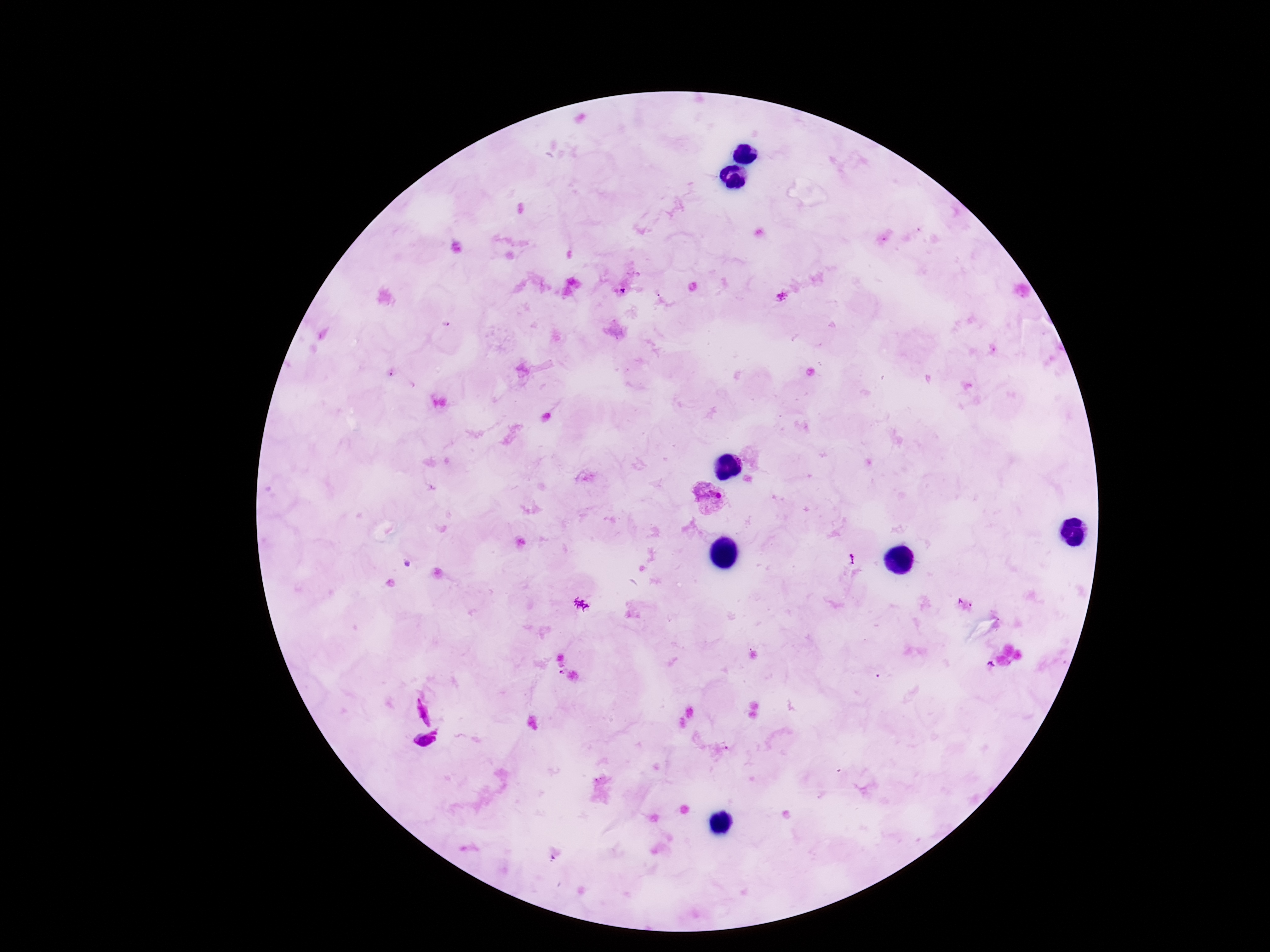

Approximate centers as {x, y} in pixels.
Summary:
  - Plasmodium parasite locations: {710, 499}
  - Field of view: one from this slide
  - Patient malaria status: positive
  - Preparation: thick blood smear
  - Image size: 1270×952 pixels
  - Magnification: 100x
  - Stain: Giemsa
  - Capture: smartphone camera through the microscope eyepiece